Assess this cell for malaria.
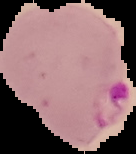

Parasitized.

The area outside the segmented cell region is set to black. From a thin blood smear. Image is 136×154 pixels.